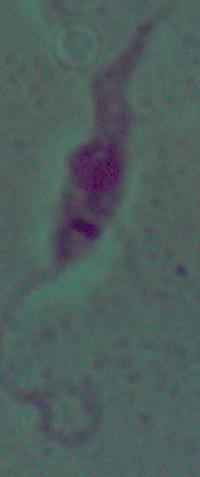

{
  "magnification": "1000x",
  "modality": "micrograph",
  "identification": "Leishmania"
}